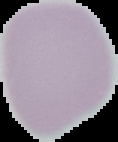

{
  "malaria_status": "uninfected",
  "preparation": "thin blood film",
  "image_type": "segmented cell region with the area outside set to black",
  "image_size": "118×142 pixels"
}